Comment on the morphology of the erythrocytes.
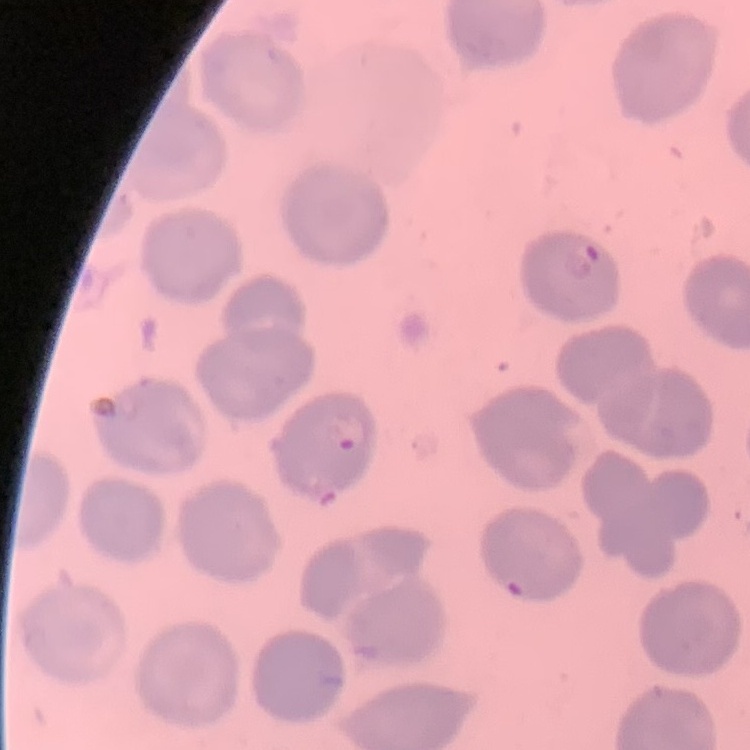

No rouleaux formation.

Thin peripheral smear. Square crop of a larger photomicrograph. Field's or Giemsa stain.